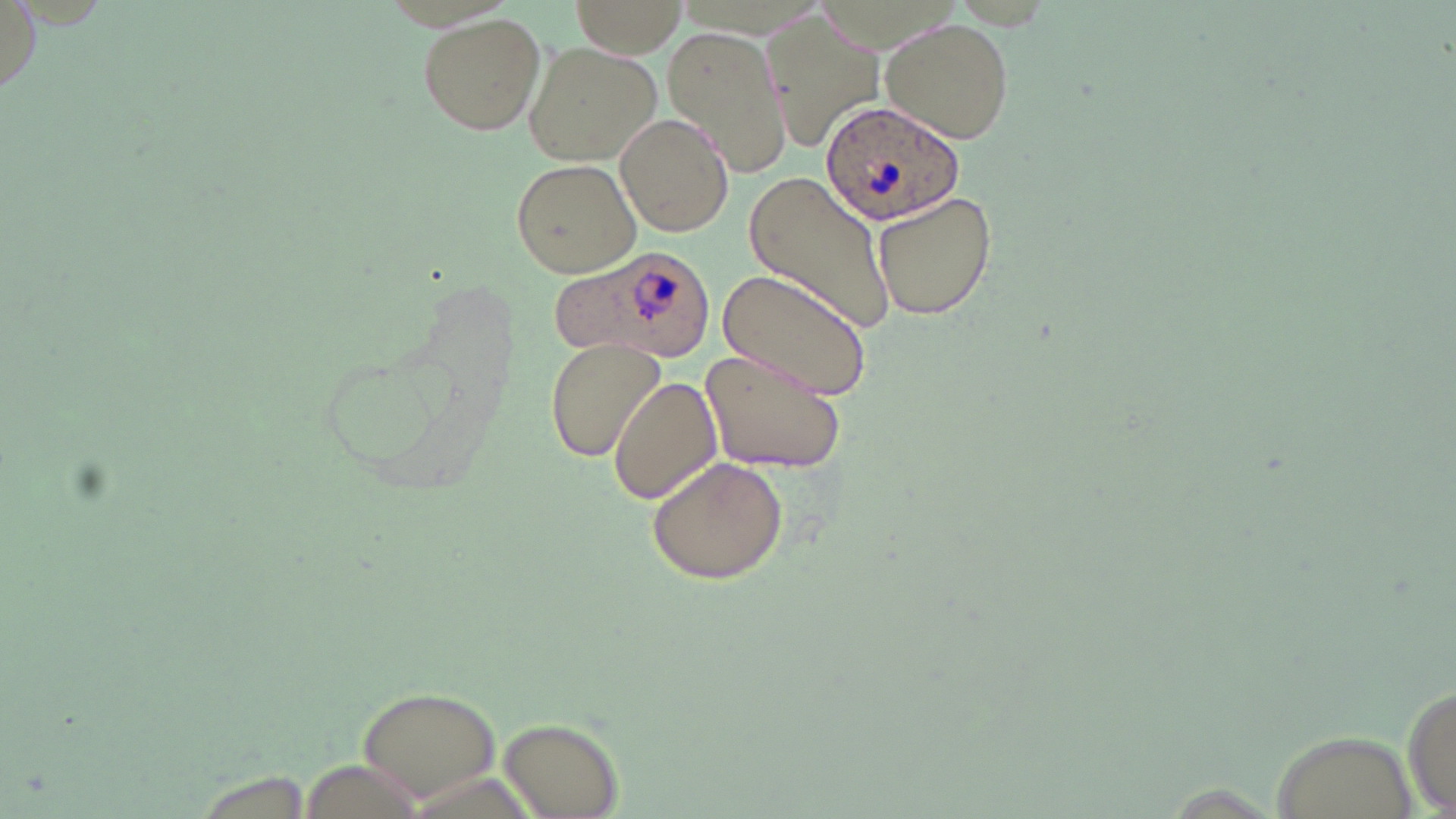
Summary:
  - Coordinate format: approximate bounding boxes as [x1, y1, x2, y2] in pixels
  - Uninfected red blood cell locations: [570, 1, 687, 60], [765, 13, 885, 152], [417, 14, 547, 136], [882, 20, 1014, 144], [663, 24, 792, 177], [523, 42, 660, 166], [615, 112, 734, 237], [511, 158, 640, 277], [742, 174, 896, 337], [872, 189, 999, 321], [716, 268, 874, 404], [544, 338, 667, 463], [699, 347, 848, 474], [609, 375, 723, 505], [647, 455, 788, 584], [1404, 677, 1455, 819], [357, 684, 502, 804], [497, 716, 624, 817]
  - Plasmodium ovale-infected red blood cell locations: [820, 102, 967, 226], [553, 244, 717, 363]
  - Slide-level diagnosis: Plasmodium ovale
  - Image size: 1456×819 pixels
  - Stain: May-Grünwald-Giemsa
  - Modality: light microscopy
  - Magnification: 1000x
  - Preparation: thin blood smear
  - Field of view: single